State the blood parasite species.
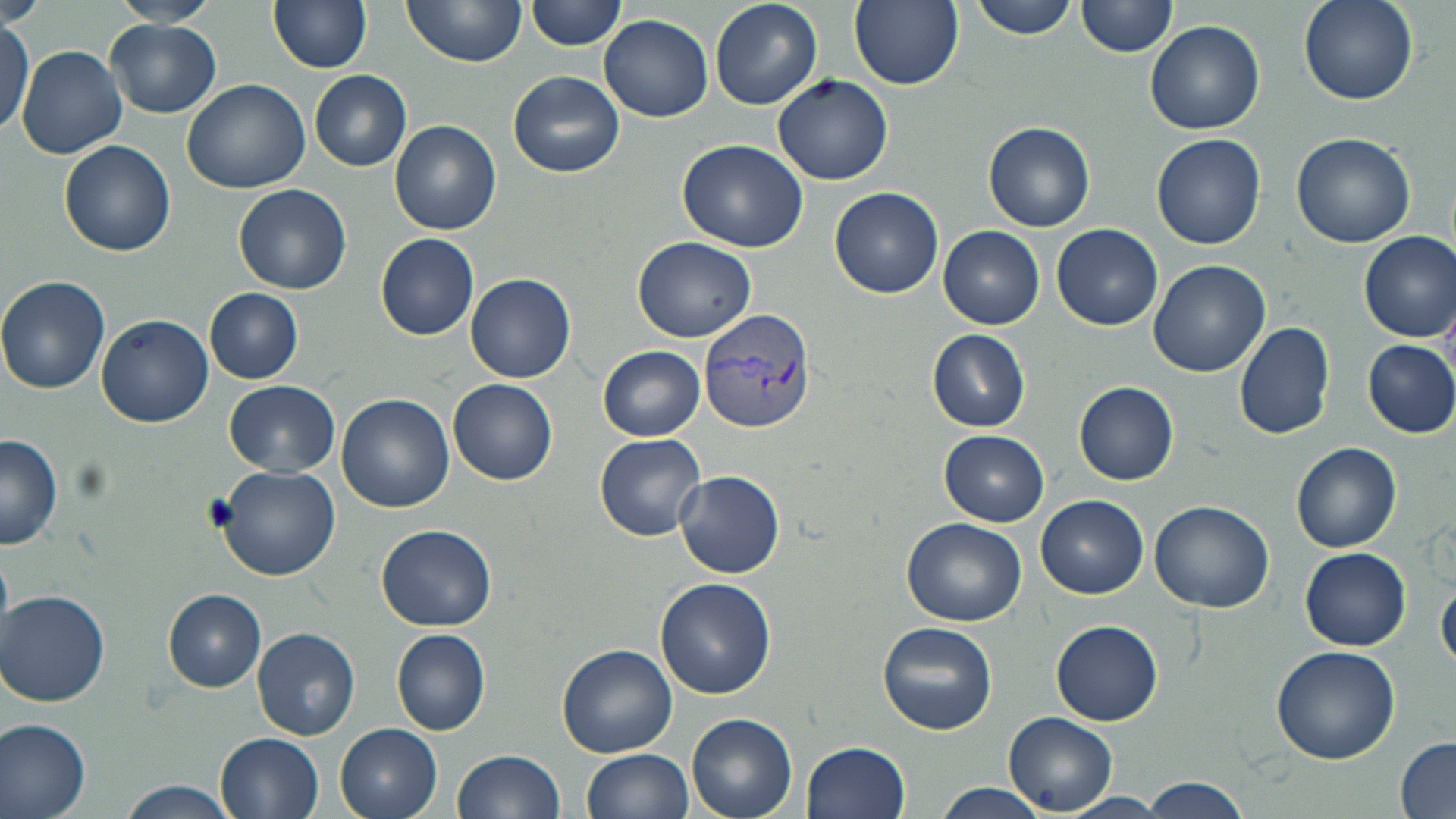

Plasmodium vivax.

Summary:
  - Coordinate format: approximate bounding boxes as [x1, y1, x2, y2] in pixels
  - Plasmodium vivax-infected red blood cell locations: [699, 307, 815, 433]
  - Uninfected red blood cell locations: [0, 0, 43, 27], [110, 0, 221, 27], [269, 0, 373, 72], [404, 0, 527, 67], [527, 0, 626, 51], [709, 0, 823, 110], [849, 0, 964, 90], [970, 0, 1083, 41], [1078, 0, 1177, 58], [1296, 0, 1416, 105], [600, 15, 714, 123], [106, 18, 221, 117], [1, 20, 33, 137], [1144, 20, 1265, 134], [18, 45, 127, 160], [508, 69, 626, 179], [311, 71, 411, 171], [773, 74, 893, 186], [181, 78, 313, 194], [390, 121, 500, 235], [984, 121, 1095, 232], [1290, 131, 1417, 248], [1152, 133, 1265, 250], [677, 139, 807, 252], [59, 141, 176, 256], [233, 184, 352, 296], [830, 186, 942, 297], [1051, 222, 1163, 331], [938, 225, 1044, 328], [1358, 232, 1456, 341], [376, 234, 479, 339], [632, 236, 756, 344], [1148, 260, 1270, 379], [465, 274, 576, 382], [0, 276, 110, 395], [204, 287, 305, 383], [96, 313, 214, 426], [1232, 322, 1335, 440], [927, 330, 1031, 432], [1360, 338, 1456, 438], [600, 346, 705, 440], [449, 379, 558, 486], [225, 381, 342, 478], [1075, 381, 1178, 486], [337, 394, 454, 512], [927, 430, 1044, 620], [938, 430, 1050, 526], [595, 432, 706, 541], [0, 434, 63, 549], [1292, 441, 1404, 552], [217, 466, 338, 579], [674, 469, 785, 579], [1037, 494, 1148, 599], [1148, 500, 1276, 613], [903, 517, 1027, 626], [377, 524, 495, 632], [1300, 548, 1412, 650], [1436, 576, 1456, 669], [656, 578, 777, 699], [163, 589, 267, 691], [1, 590, 110, 706], [1050, 618, 1164, 726], [877, 621, 997, 734], [253, 627, 360, 740], [391, 628, 490, 734], [555, 645, 678, 758], [1270, 646, 1401, 764], [1006, 712, 1117, 814], [686, 713, 798, 819], [0, 716, 91, 819], [335, 724, 444, 819], [216, 733, 324, 818], [1396, 737, 1456, 815], [803, 741, 912, 819], [584, 748, 694, 818], [452, 749, 565, 819], [1141, 777, 1251, 819], [117, 780, 238, 819], [932, 782, 1050, 819], [1061, 793, 1173, 818]
  - Image size: 1456×819 pixels
  - Field of view: one of a larger specimen
  - Preparation: thin blood smear
  - Magnification: 1000x
  - Modality: optical microscopy
  - Stain: May-Grünwald-Giemsa